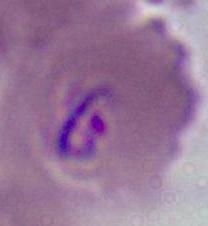
identification: Plasmodium
modality: photomicrograph
magnification: 400x or 1000x